Assess this cell for malaria.
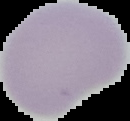

It is uninfected.

From a thin blood smear. Image is 130×121 pixels. Segmented cell region on a black background.